Classify this cell by malaria status.
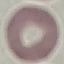
Uninfected.

Acquired by smartphone through the microscope eyepiece. Automatically extracted cell patch, resized to 64 × 64 pixels. Thin blood film. Giemsa-stained preparation.